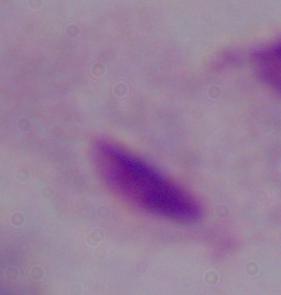
modality = micrograph
magnification = 1000x
identification = trichomonad